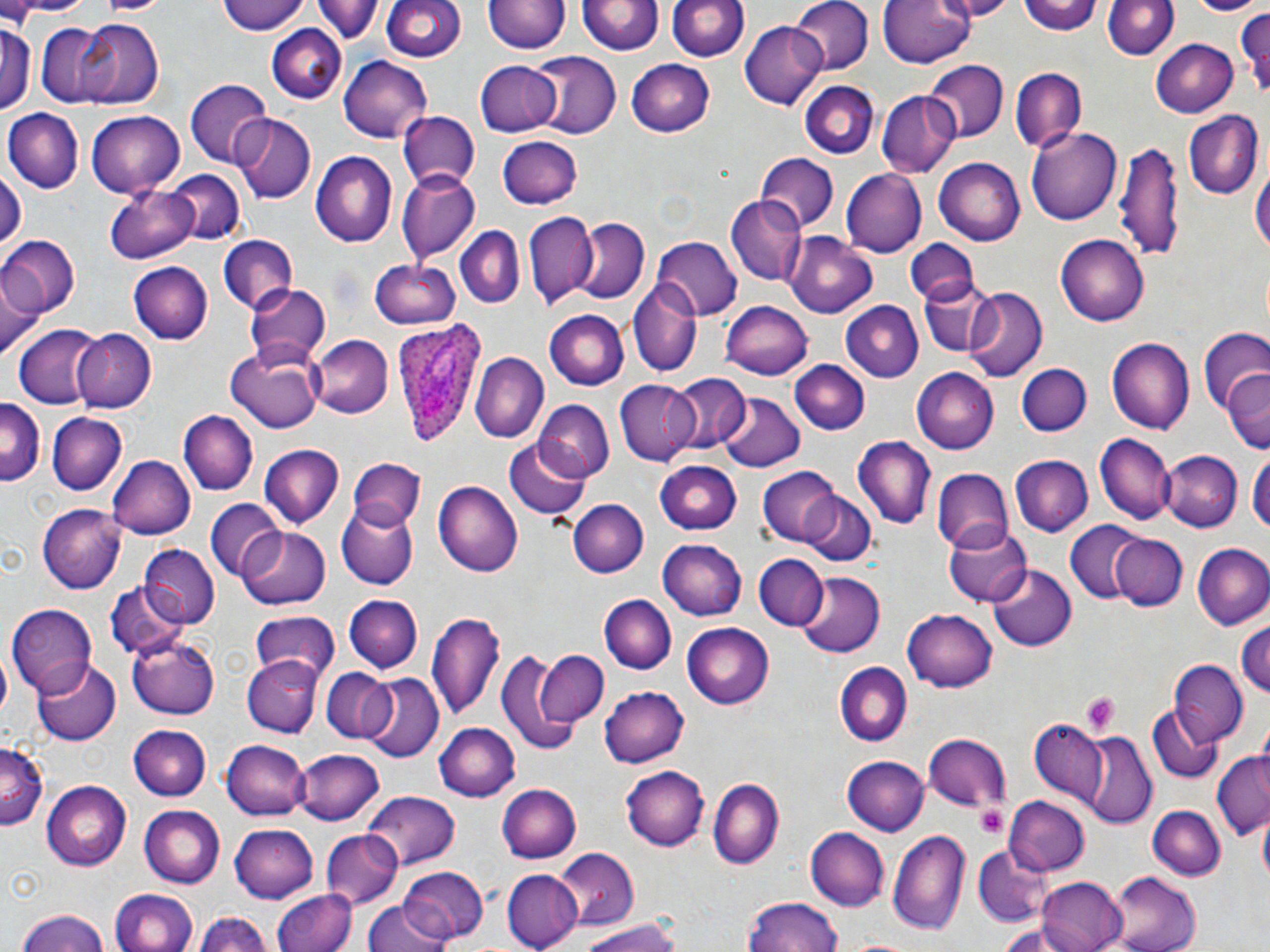
Summary:
  - Coordinate format: approximate bounding boxes as (x1,y1)-(x2,y2) corner pairs in pixels
  - Uninfected red blood cell locations: (3,0)-(98,18), (216,0)-(309,36), (318,0)-(381,44), (372,0)-(542,57), (381,0)-(464,63), (792,0)-(872,75), (880,0)-(977,69), (934,0)-(1019,19), (1021,0)-(1102,35), (1097,0)-(1177,60), (1185,0)-(1262,16), (94,1)-(174,17), (486,1)-(568,57), (668,1)-(749,63), (580,2)-(662,57), (1234,7)-(1270,98), (75,19)-(163,107), (739,21)-(828,110), (1,22)-(36,114), (34,22)-(129,107), (266,22)-(347,103), (1153,36)-(1238,116), (529,52)-(623,138), (337,54)-(434,143), (626,59)-(716,137), (924,59)-(1007,140), (474,60)-(560,137), (1011,65)-(1088,151), (802,80)-(878,158), (186,81)-(271,168), (876,90)-(959,177), (4,108)-(82,194), (86,110)-(185,197), (396,110)-(479,191), (1185,110)-(1262,198), (234,114)-(316,203), (1027,127)-(1123,225), (497,134)-(582,209), (1117,139)-(1182,264), (312,151)-(397,247), (756,153)-(838,230), (933,158)-(1025,245), (1253,163)-(1269,265), (0,167)-(23,252), (840,169)-(926,257), (163,170)-(243,248), (396,171)-(478,265), (105,184)-(197,264), (726,195)-(806,286), (523,210)-(598,306), (574,218)-(649,305), (453,226)-(524,309), (786,233)-(877,317), (1057,233)-(1149,324), (0,235)-(78,320), (216,235)-(296,317), (652,235)-(740,320), (906,236)-(979,305), (372,257)-(462,330), (127,262)-(212,344), (2,269)-(43,360), (918,280)-(1003,360), (244,282)-(331,366), (628,282)-(703,376), (962,289)-(1047,385), (721,300)-(815,378), (838,301)-(923,383), (546,310)-(628,390), (1200,323)-(1268,418), (13,324)-(103,410), (73,329)-(156,414), (311,334)-(394,417), (1107,337)-(1195,435), (225,347)-(322,433), (471,352)-(547,442), (790,361)-(871,434), (1017,363)-(1091,436), (912,369)-(998,451), (1223,370)-(1270,457), (672,373)-(750,452), (614,381)-(701,465), (717,391)-(807,473), (0,400)-(43,488), (535,401)-(616,482), (179,410)-(256,496), (46,412)-(128,496), (1094,433)-(1174,525), (853,437)-(935,529), (504,441)-(591,522), (259,446)-(343,529), (1158,448)-(1242,530), (1249,449)-(1270,540), (106,453)-(197,539), (118,455)-(206,610), (1011,455)-(1093,537), (349,459)-(425,531), (655,460)-(740,533), (758,467)-(841,545), (931,467)-(1013,553), (434,482)-(522,576), (798,492)-(875,567), (568,497)-(649,576), (206,501)-(286,581), (336,505)-(418,590), (38,506)-(126,592), (1066,519)-(1147,605), (944,524)-(1031,608), (236,525)-(332,609), (1109,533)-(1187,610), (661,540)-(746,622), (1192,542)-(1270,629), (143,546)-(219,626), (752,554)-(827,631), (988,564)-(1076,651), (794,572)-(883,657), (106,583)-(190,661), (601,594)-(676,674), (345,595)-(422,672), (8,605)-(98,695), (901,608)-(997,691), (426,609)-(505,721), (249,610)-(340,682), (1236,619)-(1270,698), (681,621)-(774,709), (129,634)-(221,719), (497,647)-(600,749), (535,651)-(607,727), (242,656)-(323,737), (33,659)-(120,745), (1168,661)-(1249,746), (836,663)-(910,746), (320,668)-(397,743), (362,675)-(443,764), (600,684)-(689,768), (1149,704)-(1222,782), (1028,719)-(1111,808), (434,721)-(520,799), (128,724)-(212,799), (1079,731)-(1155,826), (924,732)-(1009,812), (222,738)-(309,821), (1,744)-(45,827), (296,747)-(383,825), (1211,751)-(1268,841), (842,755)-(929,836), (620,764)-(709,851), (708,779)-(784,868), (40,781)-(132,867), (497,783)-(581,863), (361,793)-(460,870), (1003,796)-(1089,874), (139,804)-(226,887), (1147,805)-(1224,881), (231,822)-(318,902), (805,827)-(890,911), (887,828)-(971,938), (320,831)-(401,909), (555,846)-(641,929), (974,846)-(1049,927), (395,865)-(490,942), (503,868)-(579,949), (1108,872)-(1198,952), (1036,876)-(1128,952), (108,887)-(198,952), (272,889)-(354,952), (742,898)-(845,952), (362,900)-(454,952), (15,908)-(113,952), (195,911)-(275,952), (579,920)-(682,952)
  - Platelet locations: (1079,691)-(1119,734), (976,805)-(1006,838)
  - Plasmodium ovale-infected red blood cell locations: (391,322)-(488,448)
  - Slide-level diagnosis: Plasmodium ovale
  - Magnification: 1000x
  - Stain: May-Grünwald-Giemsa
  - Image size: 1270×952 pixels
  - Modality: light microscopy
  - Preparation: thin blood smear
  - Field of view: one of a larger specimen